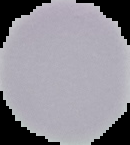
The area outside the segmented cell region is set to black. Image is 130×145 pixels. From a thin blood film. Malaria status: uninfected.